Report the malaria status of this cell.
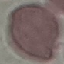

Uninfected.

Giemsa-stained preparation. Acquired by smartphone through the microscope eyepiece. Automatically extracted cell patch, resized to 64 × 64 pixels. Thin blood smear.